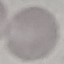
malaria status = uninfected
image type = cell patch, automatically extracted from a larger field of view and resized to 64 × 64 pixels
preparation = thin blood film
stain = Giemsa
capture = smartphone through the microscope eyepiece